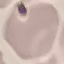
Result: no malaria parasites seen. Automatically extracted cell patch, resized to 64 × 64 pixels. Thin blood smear. Giemsa-stained preparation. Photographed with a smartphone camera at the microscope eyepiece.